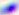

magnification: 400x
identification: Toxoplasma gondii
modality: photomicrograph